Give the extent of all Plasmodium malariae-infected red blood cells.
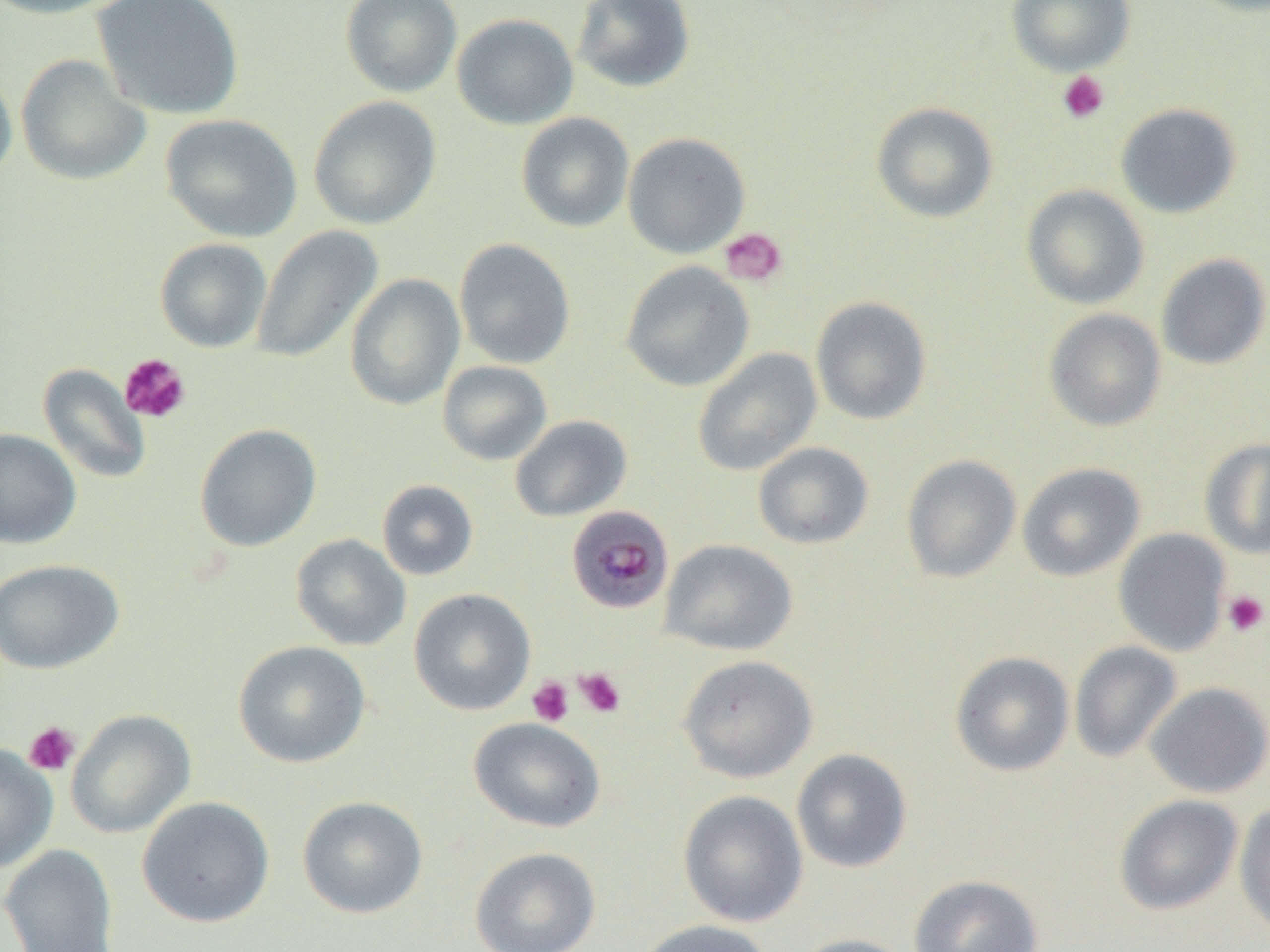

Approximate bounding boxes as (x1, y1, x2, y2) in pixels.
Plasmodium malariae-infected red blood cells: (566, 505, 674, 615).

Summary:
  - Platelet locations: (1057, 70, 1110, 124), (719, 227, 788, 287), (119, 353, 190, 423), (1222, 590, 1269, 637), (575, 668, 626, 717), (528, 677, 574, 727), (23, 721, 80, 776)
  - Uninfected red blood cell locations: (0, 0, 132, 20), (91, 0, 245, 120), (340, 0, 462, 97), (572, 0, 696, 92), (1006, 0, 1135, 76), (452, 13, 578, 130), (16, 54, 152, 186), (0, 63, 18, 188), (308, 95, 442, 229), (871, 102, 999, 223), (1115, 103, 1242, 218), (160, 113, 302, 242), (515, 113, 635, 232), (622, 132, 751, 258), (1021, 185, 1149, 310), (252, 225, 383, 364), (155, 238, 272, 352), (454, 238, 576, 369), (1156, 253, 1270, 370), (620, 261, 755, 392), (345, 273, 465, 410), (810, 296, 932, 425), (1043, 308, 1167, 432), (692, 347, 823, 477), (438, 360, 552, 465), (37, 364, 152, 484), (510, 415, 632, 522), (194, 423, 322, 552), (0, 428, 82, 549), (1199, 437, 1270, 560), (753, 441, 875, 550), (901, 454, 1021, 583), (1017, 462, 1145, 581), (377, 479, 479, 580), (1113, 528, 1231, 656), (290, 534, 411, 650), (660, 539, 798, 656), (0, 559, 124, 674), (408, 588, 537, 715), (233, 640, 371, 768), (1070, 641, 1182, 763), (950, 651, 1075, 776), (677, 654, 819, 783), (1145, 682, 1270, 798), (66, 709, 196, 838), (469, 717, 606, 833), (0, 743, 58, 873), (791, 748, 913, 873), (677, 789, 809, 927), (1114, 794, 1244, 916), (296, 795, 428, 919), (137, 796, 275, 928), (1234, 801, 1270, 939), (0, 844, 119, 952), (469, 846, 602, 952), (908, 874, 1045, 952), (634, 919, 775, 952), (787, 933, 919, 952)
  - Slide-level diagnosis: Plasmodium malariae
  - Modality: light microscopy
  - Magnification: 1000x
  - Field of view: single
  - Image size: 1270×952 pixels
  - Preparation: thin blood film